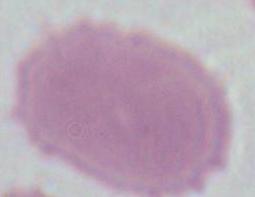

identification = erythrocyte
magnification = 1000x
modality = micrograph